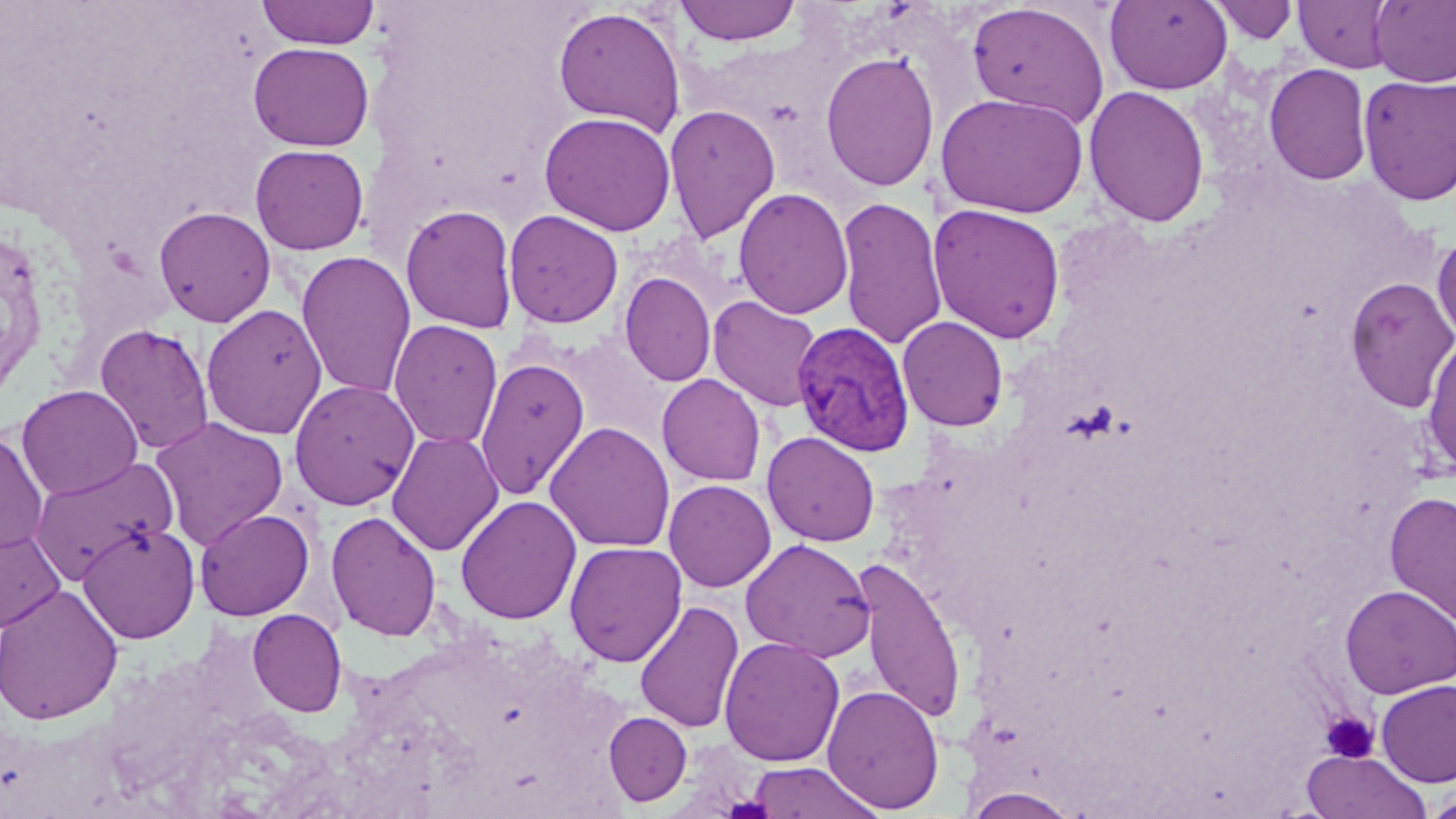
slide-level diagnosis = Plasmodium vivax
image size = 1456×819 pixels
modality = optical microscopy
magnification = 1000x
field of view = one of a larger specimen
stain = May-Grünwald-Giemsa
uninfected red blood cell locations = approximate bounding boxes as named x1/y1/x2/y2 corners in pixels: (x1=256, y1=0, x2=380, y2=49), (x1=1207, y1=0, x2=1300, y2=44), (x1=1293, y1=0, x2=1397, y2=73), (x1=1371, y1=0, x2=1456, y2=87), (x1=675, y1=1, x2=802, y2=46), (x1=1104, y1=1, x2=1233, y2=95), (x1=967, y1=2, x2=1110, y2=129), (x1=552, y1=5, x2=687, y2=136), (x1=248, y1=42, x2=374, y2=151), (x1=820, y1=50, x2=940, y2=191), (x1=1264, y1=63, x2=1372, y2=185), (x1=1358, y1=74, x2=1456, y2=205), (x1=1083, y1=85, x2=1211, y2=228), (x1=936, y1=92, x2=1089, y2=219), (x1=663, y1=103, x2=781, y2=244), (x1=539, y1=111, x2=677, y2=236), (x1=249, y1=144, x2=370, y2=255), (x1=734, y1=187, x2=854, y2=320), (x1=836, y1=195, x2=947, y2=350), (x1=400, y1=203, x2=519, y2=334), (x1=928, y1=203, x2=1066, y2=344), (x1=153, y1=205, x2=276, y2=327), (x1=502, y1=209, x2=623, y2=329), (x1=1432, y1=233, x2=1456, y2=345), (x1=296, y1=250, x2=416, y2=399), (x1=619, y1=272, x2=716, y2=387), (x1=1345, y1=276, x2=1456, y2=413), (x1=708, y1=295, x2=823, y2=412), (x1=201, y1=303, x2=327, y2=440), (x1=897, y1=316, x2=1009, y2=431), (x1=388, y1=319, x2=504, y2=449), (x1=94, y1=323, x2=215, y2=455), (x1=552, y1=329, x2=683, y2=448), (x1=1421, y1=331, x2=1456, y2=478), (x1=475, y1=357, x2=590, y2=499), (x1=657, y1=374, x2=766, y2=486), (x1=289, y1=379, x2=420, y2=510), (x1=16, y1=384, x2=143, y2=500), (x1=150, y1=415, x2=289, y2=550), (x1=544, y1=421, x2=675, y2=552), (x1=0, y1=429, x2=48, y2=555), (x1=386, y1=430, x2=504, y2=556), (x1=762, y1=431, x2=881, y2=547), (x1=28, y1=455, x2=180, y2=584), (x1=663, y1=479, x2=776, y2=592), (x1=1384, y1=490, x2=1456, y2=627), (x1=455, y1=495, x2=582, y2=624), (x1=194, y1=508, x2=314, y2=620), (x1=326, y1=510, x2=442, y2=641), (x1=77, y1=521, x2=201, y2=643), (x1=0, y1=523, x2=67, y2=634), (x1=740, y1=538, x2=876, y2=663), (x1=564, y1=541, x2=687, y2=667), (x1=855, y1=557, x2=967, y2=726), (x1=0, y1=583, x2=124, y2=726), (x1=1340, y1=584, x2=1456, y2=698), (x1=634, y1=600, x2=745, y2=734), (x1=247, y1=609, x2=347, y2=717), (x1=718, y1=636, x2=845, y2=766), (x1=1375, y1=679, x2=1456, y2=787), (x1=822, y1=683, x2=944, y2=813), (x1=603, y1=712, x2=692, y2=806), (x1=1301, y1=749, x2=1432, y2=819), (x1=746, y1=761, x2=884, y2=819), (x1=962, y1=787, x2=1082, y2=819), (x1=1423, y1=793, x2=1456, y2=819)
Plasmodium vivax-infected red blood cell locations = approximate bounding boxes as named x1/y1/x2/y2 corners in pixels: (x1=791, y1=322, x2=915, y2=457)
platelet locations = approximate bounding boxes as named x1/y1/x2/y2 corners in pixels: (x1=1319, y1=710, x2=1379, y2=763)
preparation = thin blood film